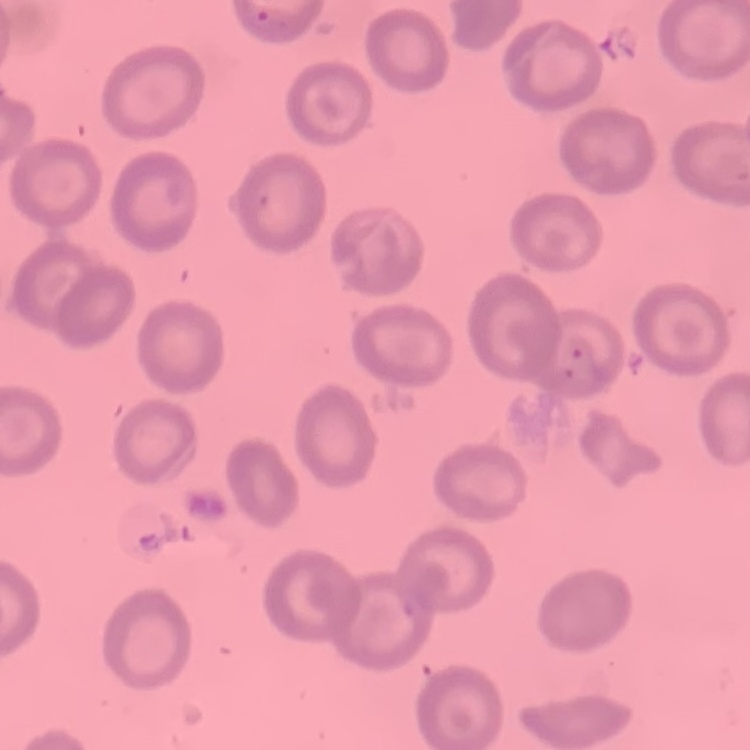 The red blood cells exhibit no rouleaux formation. Stained with either Field's or Giemsa. Square crop of a larger photomicrograph. Thin blood smear.